Locate every Plasmodium parasite.
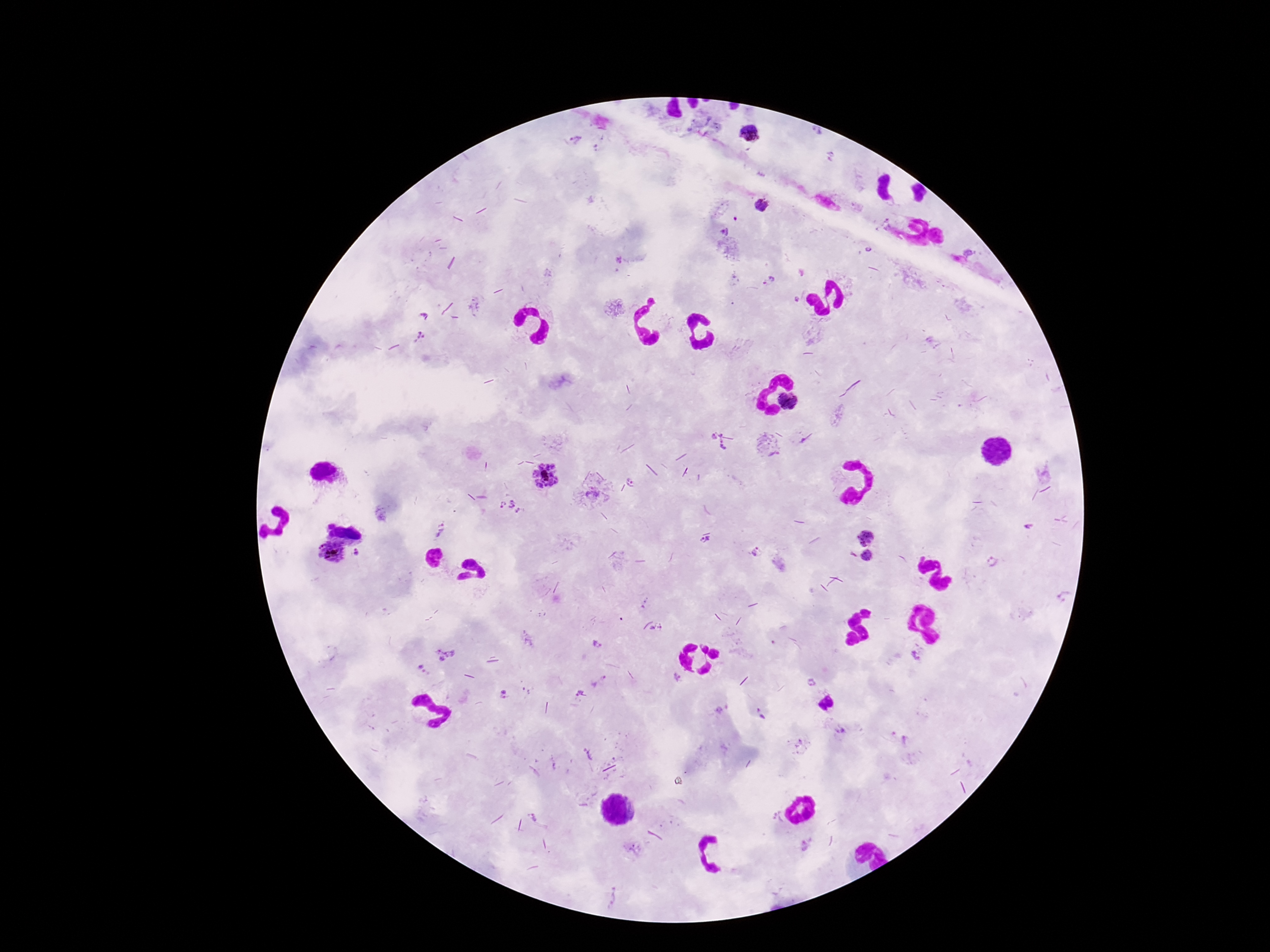
Approximate centers as {x, y} in pixels.
Plasmodium parasites: {816, 132}, {752, 134}, {576, 139}, {830, 156}, {762, 205}, {735, 218}, {724, 230}, {768, 281}, {796, 299}, {425, 316}, {420, 337}, {789, 402}, {719, 443}, {546, 479}, {632, 481}, {592, 492}, {509, 508}, {1027, 528}, {440, 530}, {706, 539}, {866, 539}, {357, 551}, {331, 552}, {756, 552}, {867, 557}, {992, 560}, {1064, 596}, {652, 628}, {596, 644}, {445, 655}, {915, 656}, {422, 667}, {677, 677}, {599, 681}, {812, 682}, {503, 694}, {581, 694}, {718, 709}, {758, 710}, {763, 717}, {840, 731}, {800, 742}, {778, 816}, {534, 818}, {806, 843}, {632, 848}, {611, 896}.

Patient malaria status: infected. 100x magnification. Photographed through the microscope eyepiece with a smartphone camera. Image is 1270×952 pixels. Giemsa stain. Thick blood film. Single field of view.